Mark where platelets are.
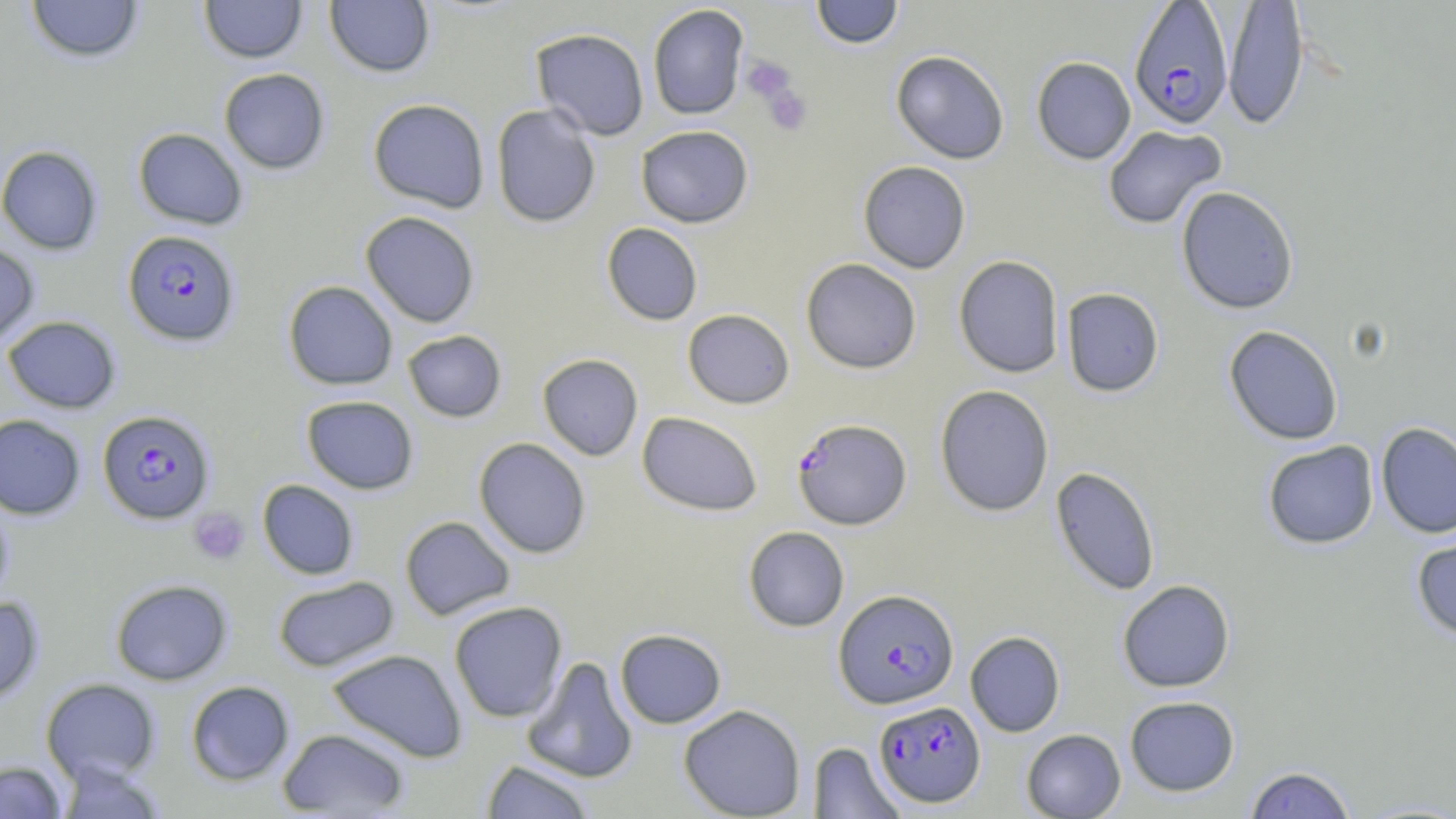
Approximate bounding boxes as [x1, y1, x2, y2] in pixels.
Platelets: [741, 55, 797, 106], [762, 83, 812, 135], [188, 507, 250, 565].

Summary:
  - Uninfected red blood cell locations: [26, 0, 144, 64], [199, 0, 307, 63], [325, 0, 435, 78], [811, 0, 904, 49], [1222, 1, 1310, 132], [647, 4, 749, 120], [530, 28, 650, 140], [890, 50, 1010, 164], [1031, 57, 1136, 164], [219, 68, 330, 174], [368, 98, 490, 212], [491, 104, 601, 228], [635, 125, 754, 228], [1102, 125, 1226, 230], [133, 127, 248, 230], [0, 145, 103, 254], [858, 160, 971, 273], [1176, 186, 1299, 314], [360, 211, 480, 328], [601, 222, 703, 325], [0, 241, 39, 348], [953, 255, 1064, 378], [801, 258, 922, 374], [283, 280, 398, 390], [1061, 287, 1164, 397], [682, 308, 795, 409], [3, 315, 121, 413], [1224, 325, 1343, 445], [402, 330, 507, 423], [537, 353, 643, 460], [934, 384, 1054, 516], [301, 395, 419, 494], [637, 411, 763, 516], [0, 414, 85, 519], [1376, 422, 1456, 538], [474, 437, 591, 559], [1262, 440, 1379, 549], [1050, 466, 1161, 596], [257, 479, 359, 580], [0, 494, 14, 604], [400, 516, 516, 620], [743, 526, 850, 632], [1412, 532, 1456, 642], [272, 575, 399, 672], [110, 579, 233, 685], [1117, 579, 1235, 692], [0, 596, 44, 705], [449, 601, 568, 723], [615, 628, 727, 728], [965, 631, 1065, 737], [326, 648, 468, 762], [521, 656, 639, 783], [41, 678, 161, 784], [186, 680, 294, 785], [1124, 695, 1240, 796], [678, 704, 806, 819], [277, 728, 411, 817], [1021, 729, 1126, 818], [808, 742, 906, 818], [481, 759, 596, 818], [0, 761, 67, 819], [55, 761, 166, 818], [1243, 765, 1358, 818]
  - Plasmodium falciparum-infected red blood cell locations: [1129, 1, 1233, 129], [122, 230, 240, 346], [97, 409, 215, 524], [792, 417, 911, 530], [834, 588, 958, 709], [874, 701, 986, 807]
  - Slide-level diagnosis: Plasmodium falciparum
  - Stain: May-Grünwald-Giemsa
  - Field of view: one of a larger specimen
  - Image size: 1456×819 pixels
  - Modality: optical microscopy
  - Preparation: thin blood film
  - Magnification: 1000x